Point out each malaria parasite and each leukocyte.
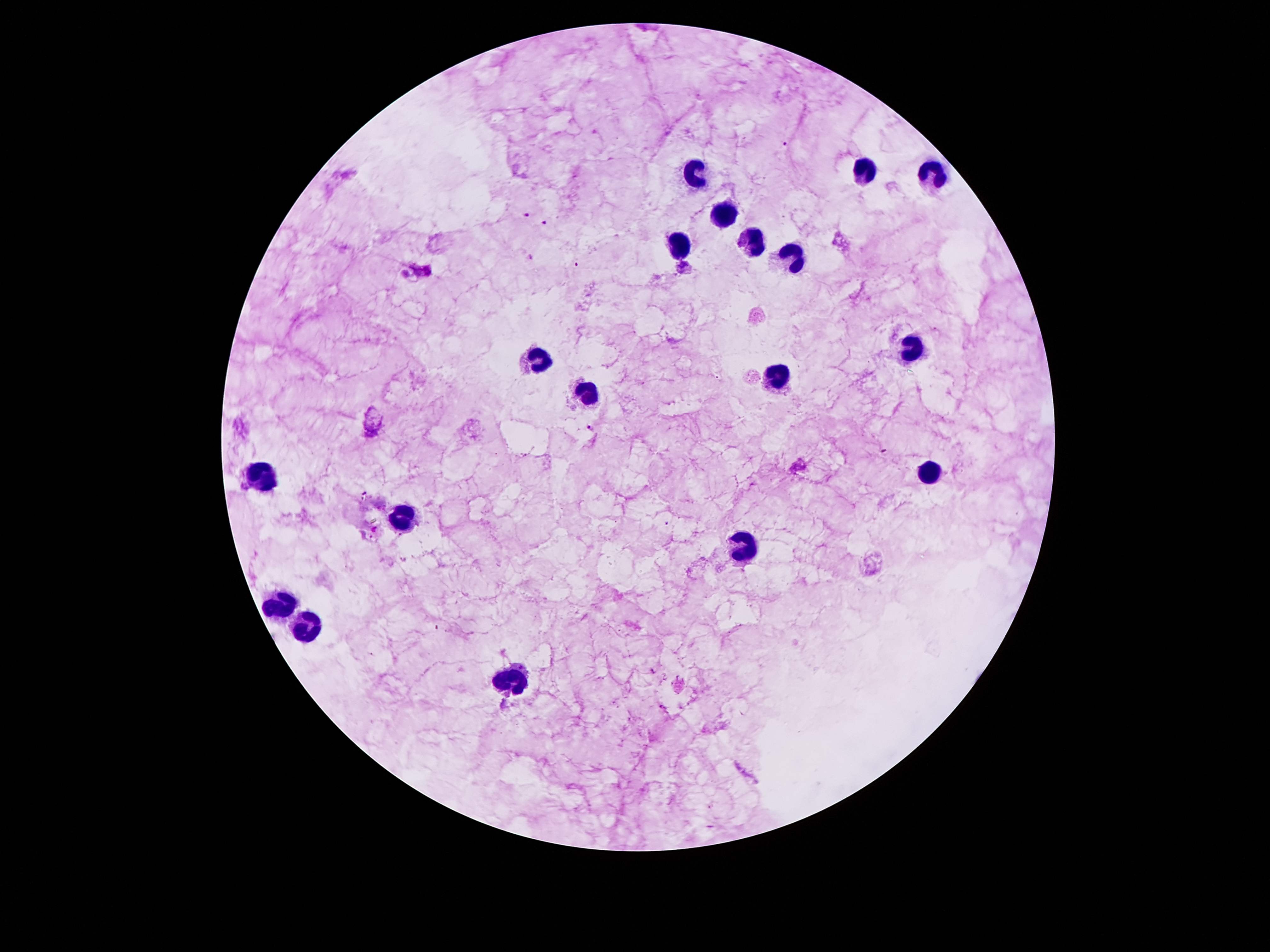

Approximate object centers, in pixels from the top-left corner.
Malaria parasites: (x=785, y=142), (x=527, y=215), (x=546, y=223), (x=531, y=258), (x=576, y=264), (x=590, y=427), (x=365, y=493), (x=666, y=524).
Leukocytes: (x=858, y=169), (x=690, y=171), (x=928, y=174), (x=723, y=216), (x=755, y=243), (x=680, y=245), (x=792, y=265), (x=913, y=342), (x=535, y=361), (x=774, y=379), (x=587, y=396), (x=928, y=470), (x=260, y=482), (x=399, y=517), (x=745, y=548), (x=278, y=609), (x=307, y=627), (x=512, y=680).

Summary:
  - Field of view: single
  - Magnification: 100x
  - Stain: Giemsa
  - Capture: smartphone through the microscope eyepiece
  - Patient malaria status: positive for Plasmodium falciparum
  - Image size: 1270×952 pixels
  - Preparation: thick peripheral-blood smear